Identify the parasite.
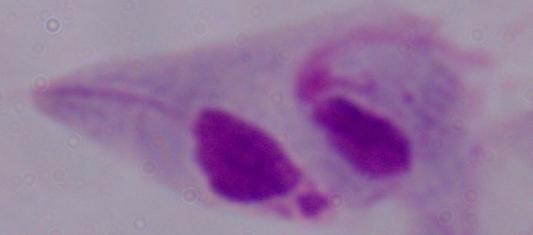

A trichomonad.

modality = photomicrograph
magnification = 1000x